Outline each Plasmodium ovale-infected red blood cell.
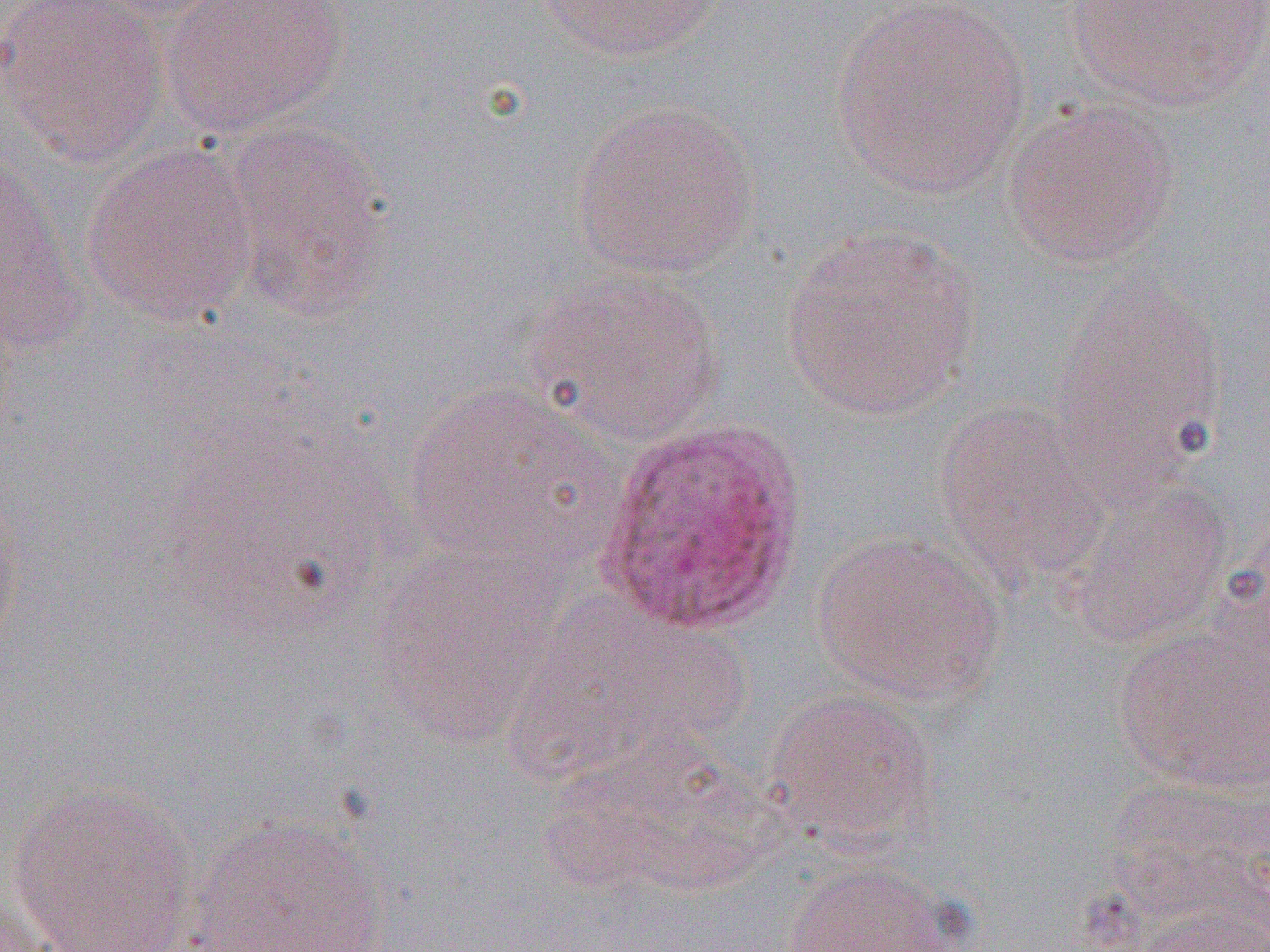

Approximate bounding boxes as (x1, y1, x2, y2) in pixels.
Plasmodium ovale-infected red blood cells: (596, 414, 812, 637).

Uninfected red blood cell locations: (1, 0, 169, 168), (83, 0, 242, 22), (161, 0, 348, 137), (534, 0, 724, 62), (1061, 0, 1268, 111), (829, 1, 1032, 199), (1001, 99, 1180, 270), (570, 100, 762, 279), (216, 119, 396, 319), (81, 140, 260, 327), (0, 152, 83, 339), (779, 225, 981, 422), (522, 265, 724, 445), (1052, 276, 1227, 485), (400, 382, 619, 573), (933, 398, 1106, 592), (1062, 474, 1233, 647), (0, 491, 24, 660), (811, 530, 1004, 704), (374, 542, 567, 746), (513, 600, 746, 780), (1112, 621, 1270, 794), (763, 688, 939, 853), (538, 728, 780, 897), (9, 781, 201, 952), (184, 813, 388, 951), (782, 860, 967, 952), (0, 891, 57, 952), (1130, 906, 1270, 952). Slide-level diagnosis: Plasmodium ovale. Image is 1270×952 pixels. Captured at 1000x magnification. Single field of view. Thin blood smear. Light microscopy.